Assess this cell for malaria.
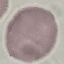

Uninfected.

Acquired by smartphone through the microscope eyepiece. Thin blood smear. Automatically extracted cell patch, resized to 64 × 64 pixels. Giemsa stain.